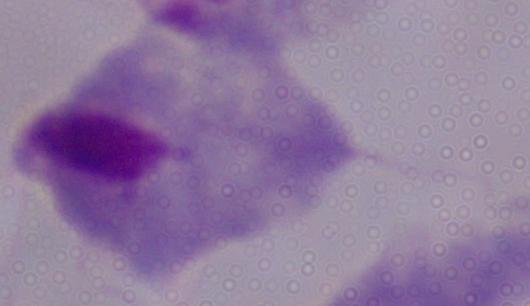

identification = trichomonad
modality = micrograph
magnification = 1000x